Locate every blood parasite and identify its species.
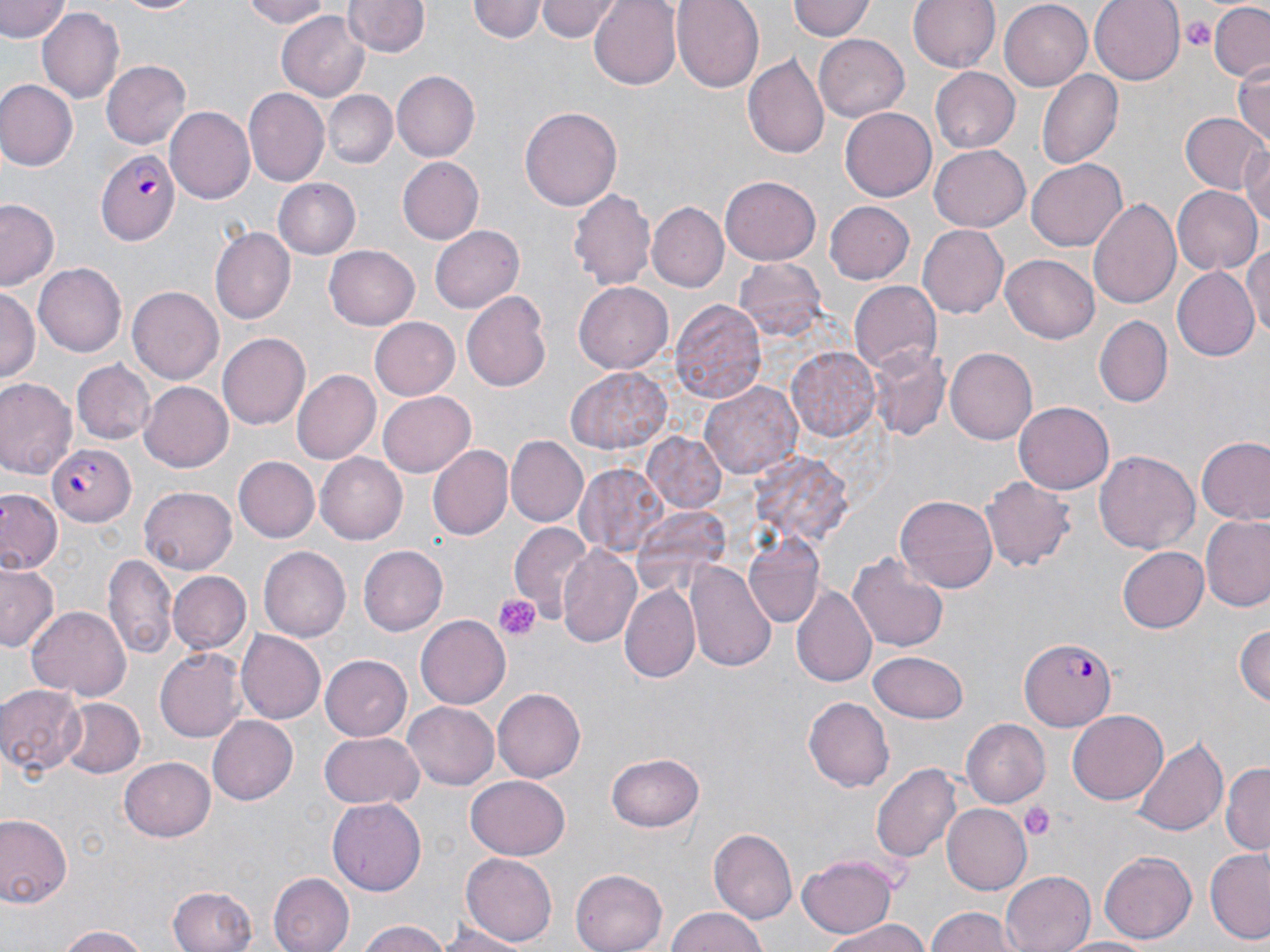
Approximate bounding boxes as (x1,y1)-(x2,y2) corner pairs in pixels.
Plasmodium falciparum-infected red blood cells: (98,149)-(178,244), (47,443)-(138,526), (1019,638)-(1120,730).
No Plasmodium ovale, Plasmodium malariae, Plasmodium vivax, Babesia divergens, or Trypanosoma brucei observed.

Summary:
  - Platelet locations: (1178,14)-(1215,52), (495,593)-(539,641), (1020,801)-(1055,839)
  - Uninfected red blood cell locations: (0,0)-(69,43), (101,0)-(207,15), (236,0)-(333,29), (471,0)-(544,43), (535,0)-(622,41), (589,0)-(683,89), (673,0)-(765,91), (789,0)-(875,43), (907,0)-(1001,74), (1089,0)-(1184,84), (345,1)-(430,57), (998,2)-(1094,91), (1207,3)-(1270,82), (39,7)-(124,104), (278,10)-(369,100), (814,31)-(910,121), (743,55)-(830,161), (1231,58)-(1270,149), (102,60)-(192,148), (929,65)-(1019,151), (1038,69)-(1123,170), (393,70)-(480,162), (0,80)-(77,170), (246,88)-(331,185), (325,89)-(397,168), (519,106)-(623,211), (840,106)-(939,202), (167,107)-(254,205), (1181,112)-(1268,196), (928,144)-(1030,232), (1243,147)-(1270,233), (396,156)-(484,245), (1027,160)-(1126,249), (722,176)-(820,264), (273,177)-(360,258), (1172,186)-(1260,276), (567,187)-(656,290), (1089,197)-(1181,311), (824,199)-(915,284), (0,202)-(59,289), (647,202)-(728,294), (917,224)-(1007,317), (431,226)-(523,312), (212,227)-(298,325), (1245,243)-(1270,342), (324,246)-(419,330), (1001,255)-(1100,343), (735,258)-(829,341), (37,262)-(127,357), (1170,267)-(1259,362), (576,282)-(673,373), (850,282)-(940,375), (0,287)-(38,383), (127,287)-(224,384), (462,292)-(556,392), (670,299)-(765,402), (1094,315)-(1173,408), (371,317)-(461,402), (219,333)-(309,429), (866,345)-(952,442), (786,346)-(880,443), (945,347)-(1037,445), (72,360)-(156,444), (566,368)-(673,454), (293,371)-(380,462), (0,377)-(76,478), (703,381)-(800,480), (140,382)-(233,473), (379,391)-(476,477), (1014,402)-(1114,493), (641,433)-(729,514), (506,436)-(588,527), (1197,437)-(1270,524), (426,443)-(513,540), (1094,451)-(1199,554), (315,452)-(409,545), (232,457)-(319,543), (576,464)-(666,556), (981,475)-(1074,572), (138,486)-(237,575), (1,492)-(61,574), (896,493)-(998,592), (1201,516)-(1270,611), (509,521)-(593,626), (742,534)-(827,629), (358,545)-(448,636), (556,545)-(643,650), (1118,546)-(1210,632), (260,547)-(349,642), (848,550)-(949,655), (107,555)-(177,664), (688,561)-(776,673), (0,562)-(61,653), (169,571)-(252,655), (620,583)-(701,684), (792,585)-(877,687), (27,606)-(131,701), (417,615)-(510,710), (1234,619)-(1269,710), (235,629)-(326,725), (154,647)-(247,743), (868,649)-(970,722), (321,655)-(412,742), (0,683)-(88,778), (494,687)-(589,783), (803,694)-(893,789), (58,698)-(144,780), (403,702)-(500,790), (1068,711)-(1167,805), (208,715)-(299,805), (963,719)-(1050,806), (319,732)-(423,808), (1130,734)-(1228,838), (607,752)-(705,832), (120,756)-(215,841), (1222,763)-(1270,853), (872,765)-(960,863), (466,773)-(570,859), (327,798)-(426,896), (944,801)-(1035,896), (0,813)-(72,909), (709,828)-(798,924), (1205,848)-(1270,943), (1099,849)-(1198,944), (463,852)-(556,946), (798,853)-(897,937), (569,866)-(668,952), (1001,871)-(1094,952), (268,872)-(352,952), (168,886)-(258,952), (666,907)-(768,952), (923,909)-(1023,952), (821,920)-(934,952), (357,921)-(455,952), (436,922)-(530,952), (53,925)-(156,952), (1055,936)-(1159,952)
  - Slide-level diagnosis: Plasmodium falciparum
  - Modality: optical microscopy
  - Image size: 1270×952 pixels
  - Stain: May-Grünwald-Giemsa
  - Preparation: thin blood smear
  - Magnification: 1000x
  - Field of view: one of a larger specimen